Name the malaria species.
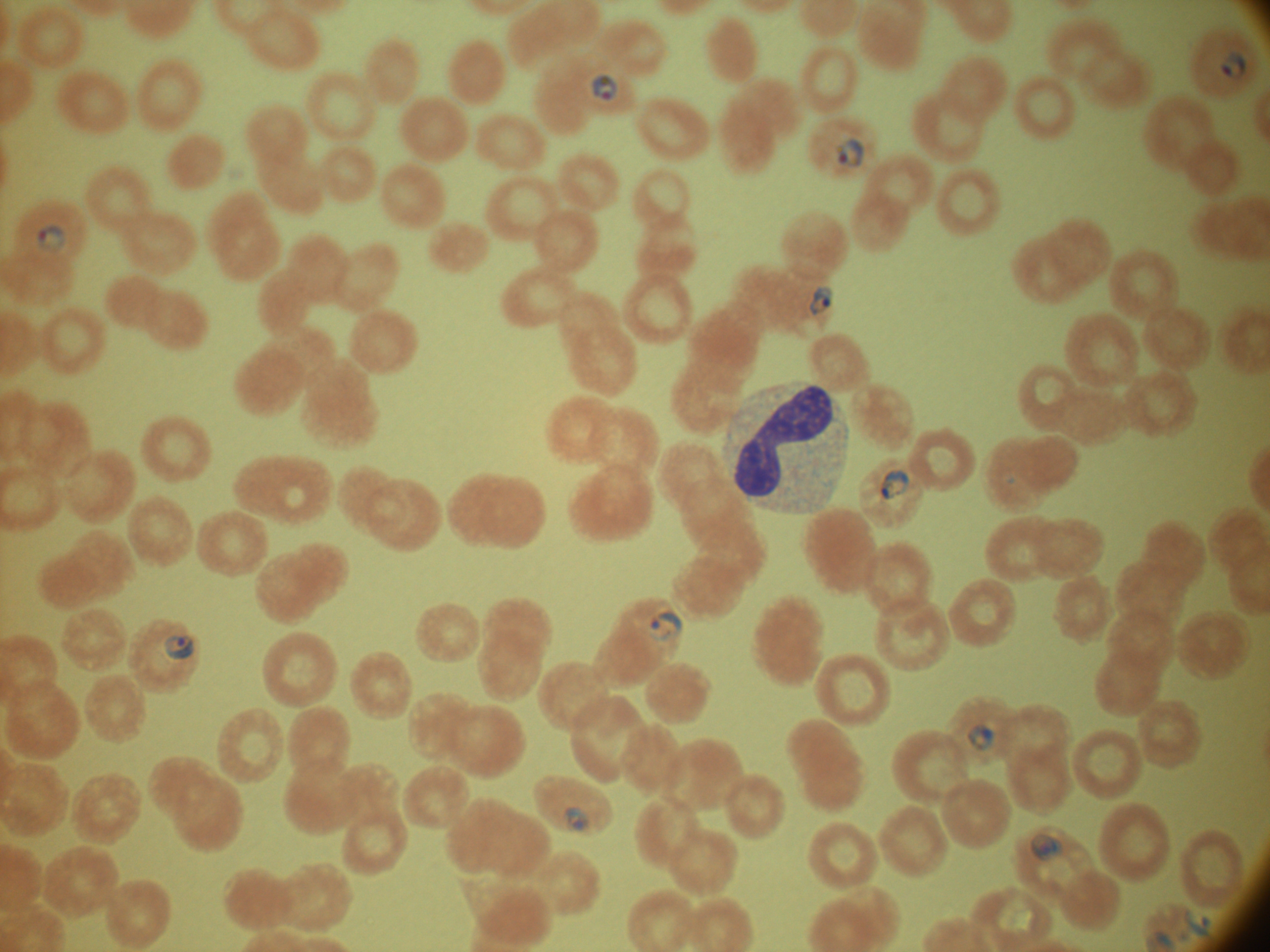
Plasmodium falciparum.

Approximate bounding boxes as [x1, y1, x2, y2] in pixels, from the source annotation, which is not necessarily exhaustive. Ring form locations: [1221, 51, 1246, 79], [592, 73, 619, 101], [836, 137, 865, 168], [36, 225, 67, 253], [809, 285, 833, 315], [880, 468, 910, 501], [649, 612, 684, 641], [164, 635, 195, 660], [967, 723, 997, 752], [564, 806, 588, 830], [1030, 834, 1062, 861], [1184, 909, 1210, 936]. Thin blood film. Single field of view. 100x magnification. Leica DM2000 optical microscope with a built-in camera. Giemsa-stained preparation. Image is 1270×952 pixels.